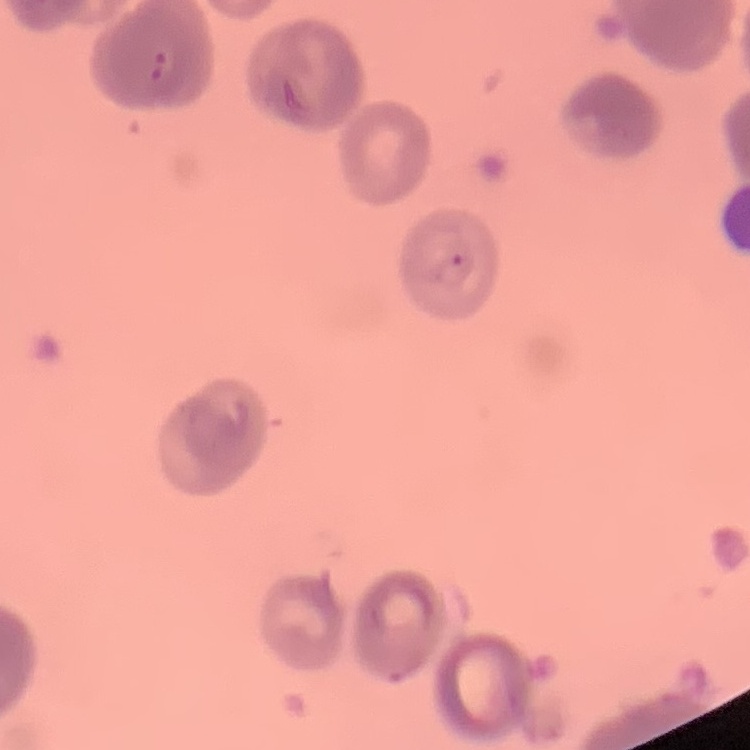

The erythrocytes exhibit rouleaux formation. Thin blood film. Stained with either Field's or Giemsa. One tile cut from a larger photomicrograph.